Give the position of each P. falciparum parasite with its life-cycle stage, each leukocyte, and any debris.
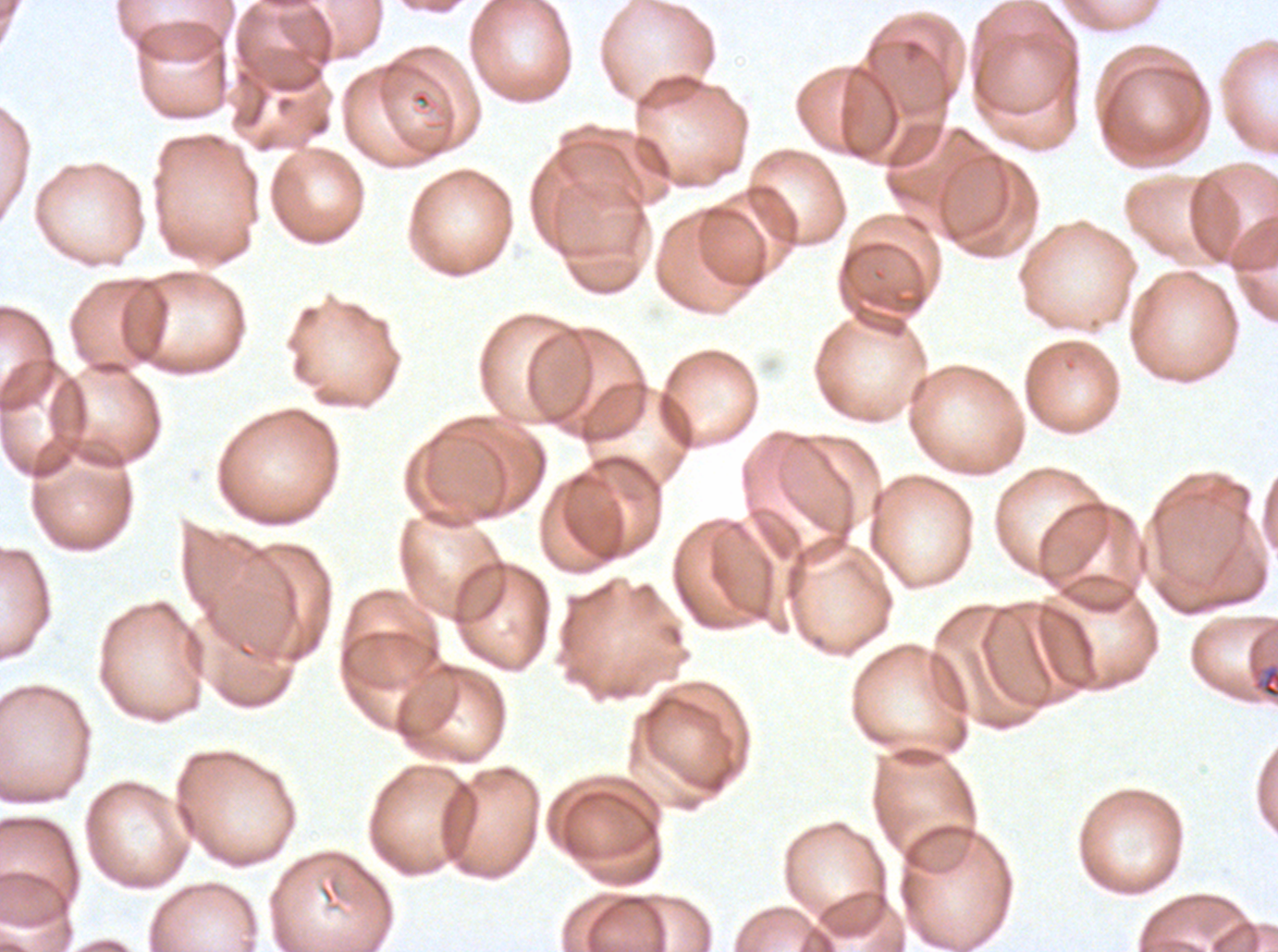

Approximate bounding boxes as [x1, y1, x2, y2] in pixels.
Debris: [1253, 664, 1277, 700].
No rings, late-ring/early-trophozoite forms, mid trophozoites, late trophozoites, early schizonts, late schizonts, segmenters, gametocytes, or leukocytes observed.

One sub-image of a larger composite. Thin blood smear. P. falciparum cultured ex vivo for 24 to 48 hours, from a patient in The Gambia. Image is 1278×952 pixels. Giemsa-stained preparation.